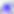

identification = Toxoplasma gondii
magnification = 400x
modality = photomicrograph